Report the malaria status of this cell.
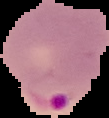
It is parasitized.

Summary:
  - Image size: 109×118 pixels
  - Image type: segmented cell region with the area outside set to black
  - Preparation: thin blood smear